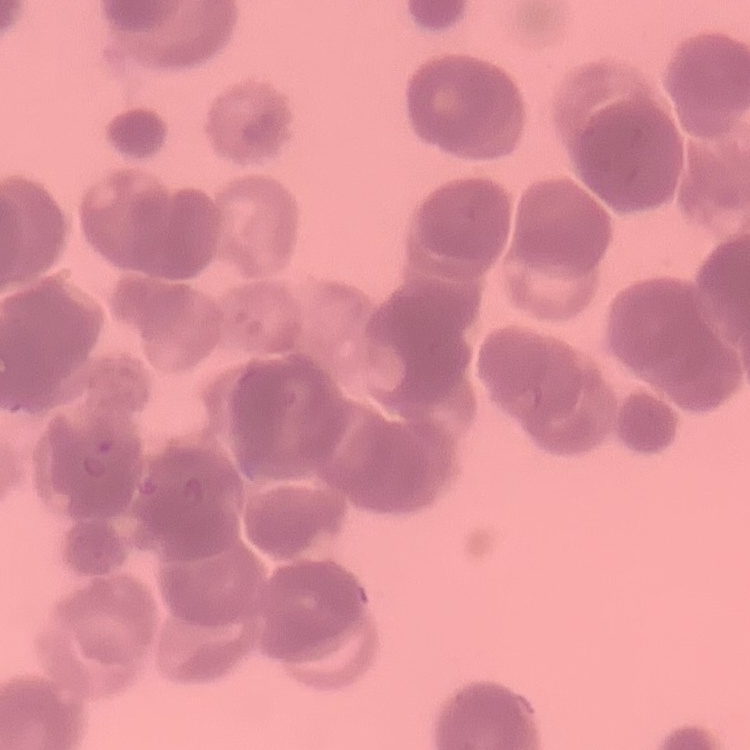
{
  "erythrocyte_morphology": "rouleaux formation",
  "image_type": "one tile cut from a larger photomicrograph",
  "stain": "Field's or Giemsa",
  "preparation": "thin blood film"
}